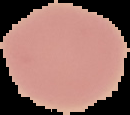
Summary:
  - Image type: segmented cell region with the area outside set to black
  - Preparation: thin blood smear
  - Result: no Plasmodium parasites seen
  - Image size: 130×115 pixels